Assess this cell for malaria.
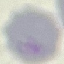
It is uninfected.

stain: Giemsa
preparation: thin blood smear
image_type: automatically extracted cell patch, resized to 64 × 64 pixels
capture: smartphone through the microscope eyepiece